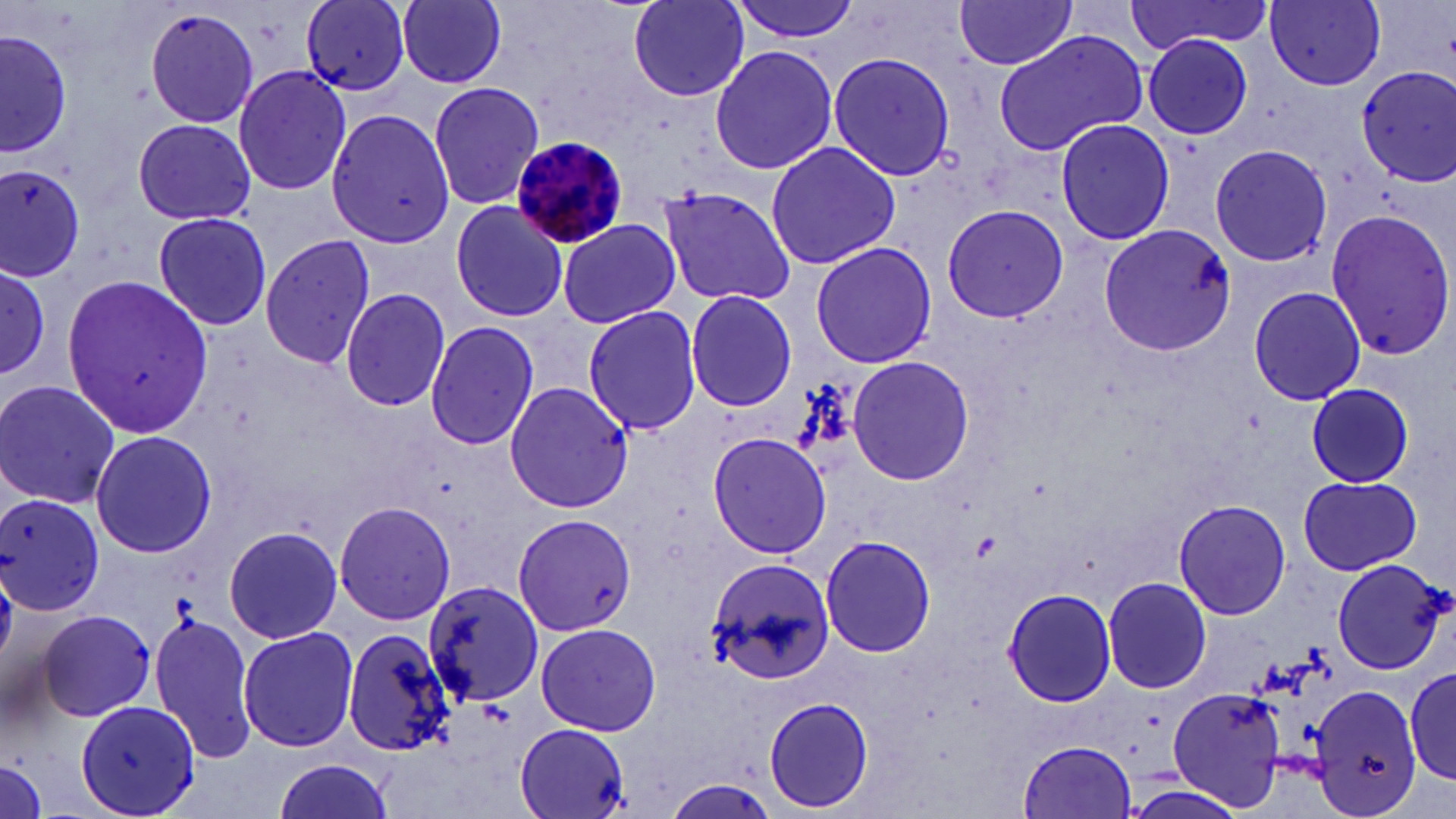

{
  "plasmodium_malariae_infected_red_blood_cell_locations": "approximate bounding boxes as (x1,y1)-(x2,y2) corner pairs in pixels: (510,135)-(632,250)",
  "slide_level_diagnosis": "Plasmodium malariae",
  "stain": "May-Grünwald-Giemsa",
  "uninfected_red_blood_cell_locations": "approximate bounding boxes as (x1,y1)-(x2,y2) corner pairs in pixels: (398,0)-(508,89), (625,0)-(753,102), (728,0)-(863,43), (1123,0)-(1276,55), (1259,0)-(1390,95), (1266,0)-(1387,90), (952,1)-(1080,71), (300,2)-(412,99), (143,8)-(261,130), (0,23)-(72,161), (992,29)-(1148,156), (1144,36)-(1254,139), (708,44)-(841,176), (826,51)-(956,181), (232,63)-(354,199), (1356,66)-(1456,188), (428,81)-(547,210), (325,109)-(459,249), (1054,116)-(1175,247), (130,117)-(260,228), (765,138)-(901,270), (1208,142)-(1333,268), (0,160)-(89,284), (660,187)-(797,306), (447,201)-(570,325), (940,205)-(1067,323), (1324,209)-(1456,362), (151,210)-(274,333), (557,218)-(681,329), (1097,224)-(1236,356), (259,235)-(375,369), (810,240)-(937,369), (0,265)-(50,374), (59,272)-(214,436), (340,286)-(450,413), (1248,286)-(1366,404), (685,289)-(798,412), (582,305)-(702,433), (425,318)-(540,452), (847,354)-(975,486), (0,379)-(121,508), (504,381)-(632,513), (1305,382)-(1414,488), (88,427)-(218,560), (705,430)-(833,560), (1296,476)-(1422,575), (0,492)-(105,616), (333,499)-(456,628), (1173,500)-(1290,620), (511,511)-(637,639), (222,525)-(342,645), (819,533)-(937,659), (703,558)-(836,687), (1331,558)-(1450,675), (1102,575)-(1212,695), (422,578)-(547,708), (1002,588)-(1117,708), (39,607)-(159,723), (149,611)-(259,765), (534,620)-(662,737), (238,626)-(361,753), (342,626)-(454,757), (1404,665)-(1456,785), (1309,682)-(1421,815), (1305,684)-(1423,817), (1169,687)-(1287,810), (763,696)-(874,814), (74,697)-(200,817), (515,725)-(632,819), (1019,739)-(1138,817), (0,753)-(48,819), (270,756)-(398,819), (661,780)-(784,819), (1119,781)-(1248,819)",
  "image_size": "1456×819 pixels",
  "preparation": "thin blood film",
  "magnification": "1000x",
  "modality": "optical microscopy",
  "field_of_view": "one of a larger specimen"
}